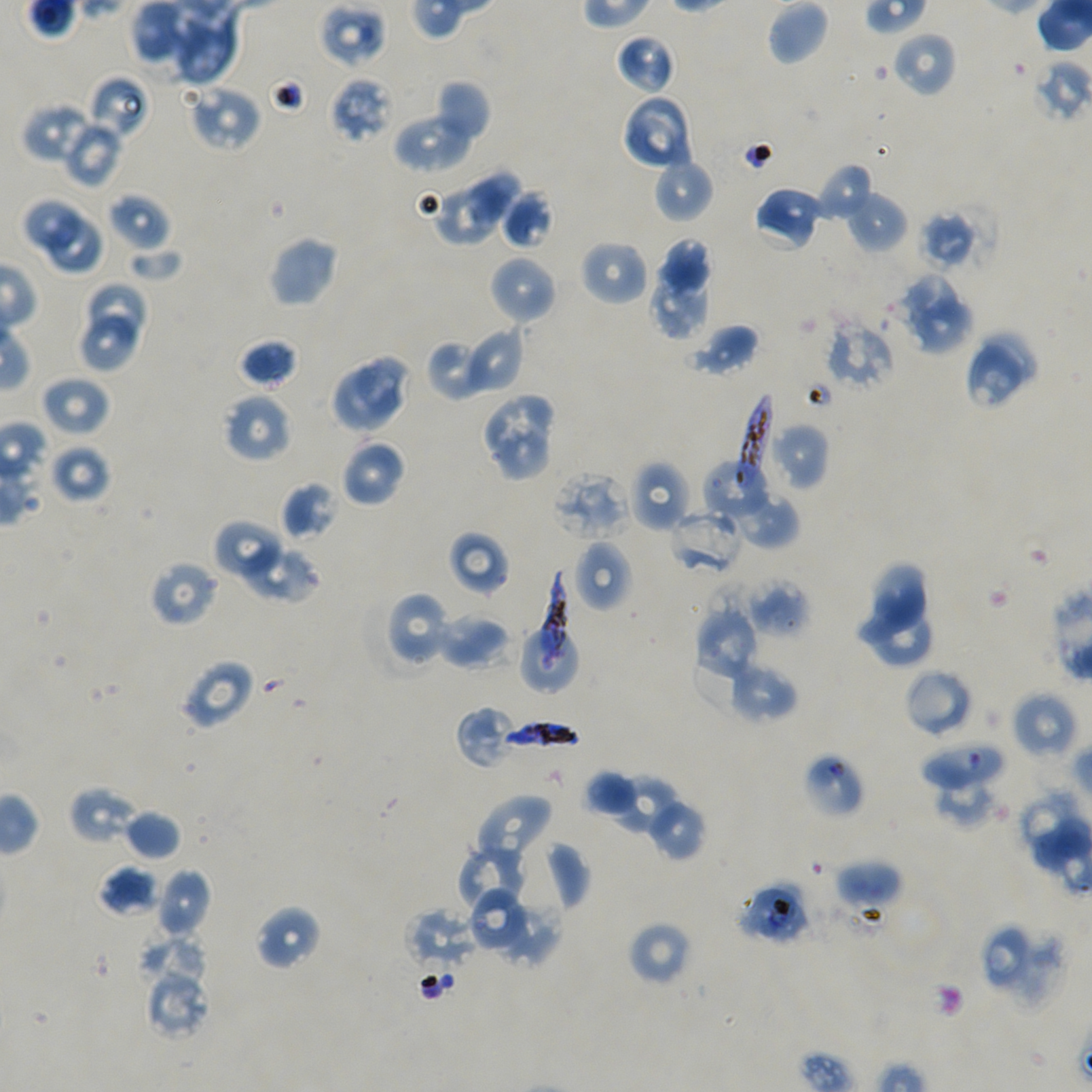
Approximate bounding boxes as [x1, y1, x2, y2] in pixels. Not every red blood cell is marked. Locations of red blood cells of indeterminate infection status: [318, 2, 388, 69], [920, 742, 1005, 793], [737, 881, 812, 945]. Locations of uninfected red blood cells: [131, 0, 187, 64], [767, 0, 830, 65], [172, 6, 240, 84], [892, 31, 956, 97], [615, 33, 676, 94], [88, 74, 151, 140], [329, 76, 393, 144], [434, 79, 490, 143], [185, 85, 261, 152], [621, 94, 695, 172], [22, 103, 96, 164], [394, 111, 475, 172], [61, 117, 124, 187], [652, 156, 714, 223], [816, 162, 875, 221], [465, 169, 518, 224], [753, 186, 824, 251], [429, 187, 500, 246], [500, 190, 553, 249], [846, 190, 907, 253], [108, 192, 171, 251], [22, 197, 81, 252], [917, 202, 994, 274], [47, 213, 109, 279], [268, 234, 340, 308], [579, 238, 649, 307], [657, 238, 713, 301], [128, 247, 185, 285], [488, 255, 557, 325], [649, 267, 712, 340], [899, 274, 960, 338], [87, 280, 147, 340], [912, 302, 975, 357], [78, 312, 141, 371], [823, 319, 894, 393], [686, 323, 760, 377], [458, 325, 524, 397], [982, 331, 1040, 385], [426, 335, 493, 402], [238, 338, 299, 390], [966, 344, 1025, 410], [358, 354, 412, 416], [328, 366, 399, 435], [41, 375, 111, 437], [222, 393, 293, 463], [484, 397, 553, 456], [767, 420, 830, 490], [495, 422, 557, 482], [340, 439, 406, 507], [48, 444, 111, 504], [703, 457, 778, 524], [629, 460, 692, 532], [550, 470, 630, 540], [280, 481, 338, 542], [729, 492, 799, 551], [668, 509, 744, 576], [213, 520, 286, 582], [448, 531, 509, 598], [238, 540, 321, 605], [572, 540, 634, 613], [149, 560, 220, 627], [861, 562, 930, 639], [746, 581, 809, 638], [382, 591, 452, 670], [695, 602, 760, 680], [872, 611, 934, 666], [436, 613, 511, 670], [520, 627, 579, 693], [692, 647, 768, 716], [178, 659, 255, 729], [727, 661, 798, 723], [904, 668, 973, 738], [1012, 691, 1078, 760], [456, 705, 519, 769], [802, 751, 865, 818], [587, 771, 640, 818], [613, 777, 679, 835], [935, 783, 1008, 831], [69, 787, 139, 845], [1016, 788, 1084, 858], [475, 794, 553, 864], [646, 797, 706, 861], [123, 809, 181, 860], [539, 840, 591, 913], [456, 844, 529, 915], [834, 859, 903, 909], [98, 864, 160, 917], [157, 867, 212, 937], [472, 888, 524, 951], [500, 900, 565, 967], [254, 905, 323, 972], [405, 907, 479, 973], [627, 920, 692, 987], [981, 922, 1069, 1008], [142, 930, 211, 993], [147, 970, 211, 1036]. Locations of infected red blood cells: [738, 392, 773, 488], [542, 570, 569, 671], [499, 719, 583, 752]. Giemsa-stained preparation. Thin blood film. Single field of view. Oil immersion, 100x objective (numerical aperture 1.45). P. falciparum strain NF54 in static in-vitro culture. Image is 1092×1092 pixels. Blood group of the donor: A+/O+.